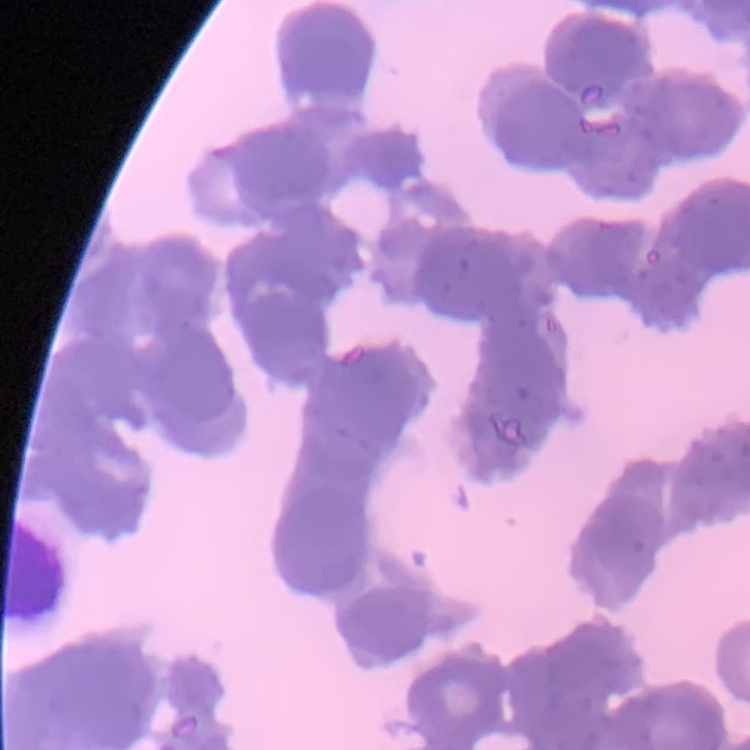
The red blood cells show rouleaux formation. Field's or Giemsa stain. Square crop of a larger photomicrograph. Thin blood smear.